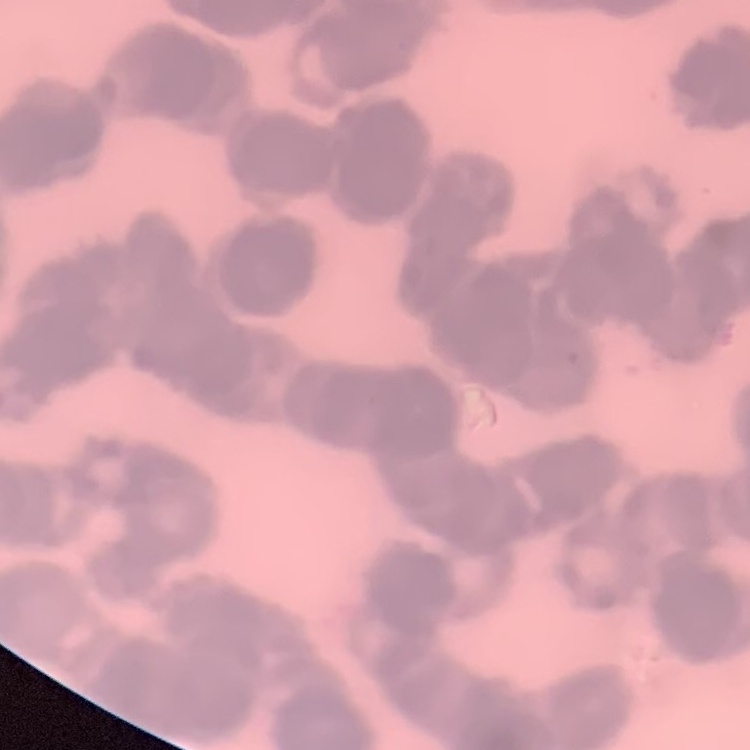
The red blood cells show rouleaux formation. Field's or Giemsa stain. One tile cut from a larger photomicrograph. Thin blood film.